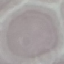
result = no malaria parasites seen
preparation = thin blood smear
image type = automatically extracted cell patch, resized to 64 × 64 pixels
capture = smartphone through the microscope eyepiece
stain = Giemsa